Name the blood parasite species.
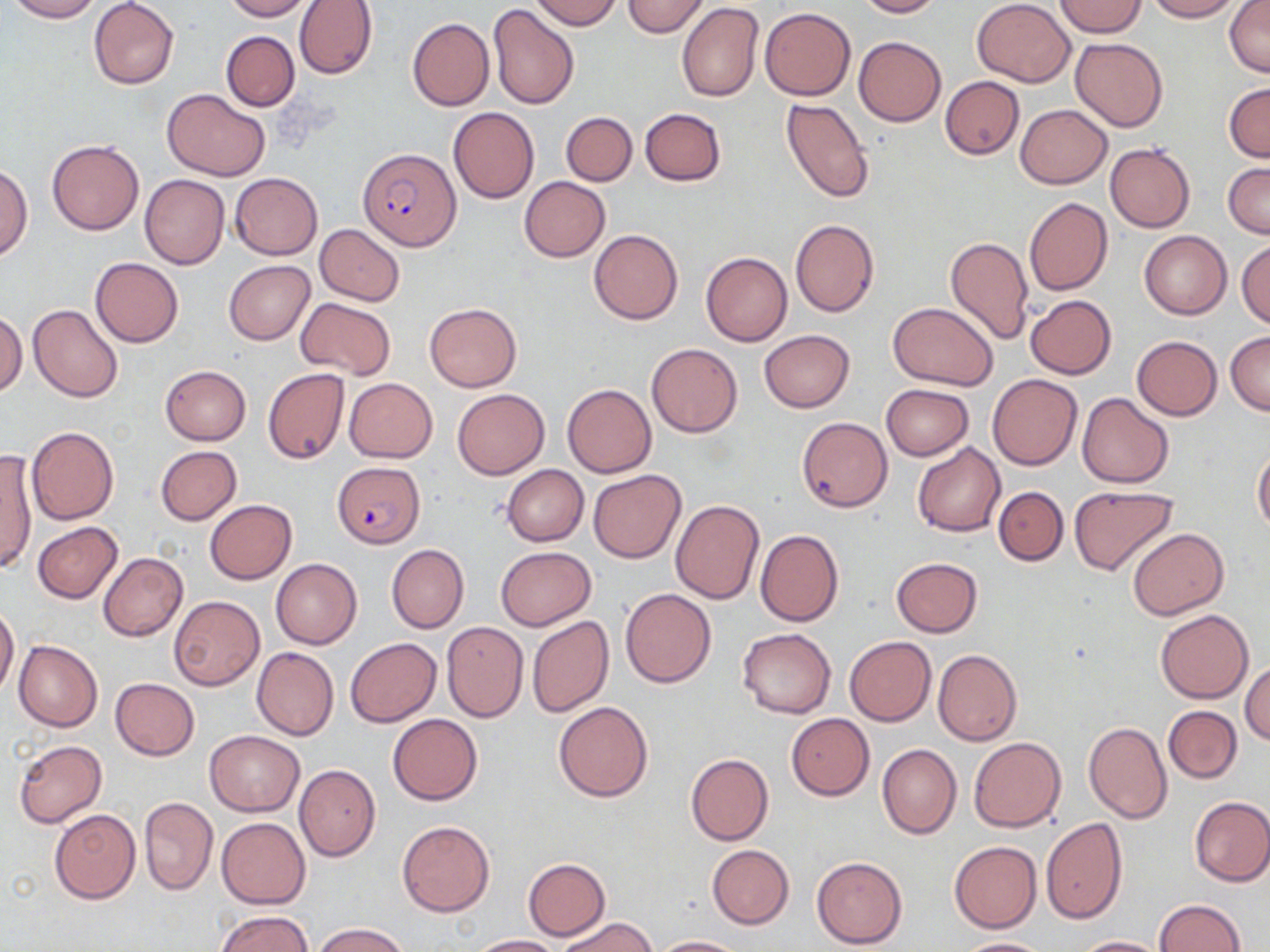

Plasmodium falciparum.

Approximate bounding boxes as named x1/y1/x2/y2 corners in pixels. Plasmodium falciparum-infected red blood cell locations: (x1=360, y1=150, x2=461, y2=251), (x1=331, y1=462, x2=422, y2=544). Uninfected red blood cell locations: (x1=6, y1=0, x2=102, y2=22), (x1=88, y1=0, x2=179, y2=89), (x1=220, y1=0, x2=311, y2=21), (x1=294, y1=0, x2=377, y2=79), (x1=529, y1=0, x2=621, y2=30), (x1=623, y1=0, x2=709, y2=37), (x1=853, y1=0, x2=942, y2=17), (x1=971, y1=0, x2=1076, y2=86), (x1=1145, y1=0, x2=1243, y2=21), (x1=1225, y1=0, x2=1270, y2=76), (x1=1054, y1=1, x2=1147, y2=37), (x1=487, y1=3, x2=579, y2=110), (x1=677, y1=3, x2=764, y2=103), (x1=761, y1=7, x2=856, y2=100), (x1=407, y1=17, x2=494, y2=111), (x1=221, y1=30, x2=299, y2=112), (x1=854, y1=36, x2=946, y2=126), (x1=1071, y1=38, x2=1168, y2=131), (x1=940, y1=76, x2=1025, y2=159), (x1=1224, y1=82, x2=1269, y2=162), (x1=162, y1=88, x2=271, y2=180), (x1=781, y1=97, x2=875, y2=203), (x1=1014, y1=105, x2=1113, y2=189), (x1=448, y1=107, x2=540, y2=203), (x1=640, y1=109, x2=726, y2=185), (x1=561, y1=112, x2=637, y2=185), (x1=47, y1=140, x2=144, y2=234), (x1=1105, y1=143, x2=1195, y2=232), (x1=1224, y1=162, x2=1269, y2=239), (x1=1, y1=164, x2=33, y2=261), (x1=230, y1=172, x2=322, y2=259), (x1=140, y1=174, x2=229, y2=270), (x1=518, y1=176, x2=610, y2=261), (x1=1024, y1=197, x2=1113, y2=295), (x1=790, y1=218, x2=878, y2=317), (x1=315, y1=225, x2=405, y2=305), (x1=590, y1=230, x2=683, y2=324), (x1=1139, y1=231, x2=1232, y2=319), (x1=945, y1=236, x2=1034, y2=344), (x1=1237, y1=239, x2=1270, y2=328), (x1=701, y1=251, x2=793, y2=346), (x1=90, y1=257, x2=183, y2=348), (x1=224, y1=260, x2=315, y2=344), (x1=1025, y1=295, x2=1117, y2=379), (x1=294, y1=298, x2=396, y2=380), (x1=424, y1=302, x2=522, y2=391), (x1=887, y1=302, x2=998, y2=389), (x1=28, y1=303, x2=123, y2=402), (x1=0, y1=312, x2=26, y2=396), (x1=759, y1=330, x2=854, y2=412), (x1=1226, y1=331, x2=1270, y2=415), (x1=1132, y1=335, x2=1223, y2=420), (x1=646, y1=342, x2=743, y2=438), (x1=160, y1=365, x2=251, y2=445), (x1=263, y1=368, x2=350, y2=464), (x1=988, y1=374, x2=1082, y2=470), (x1=343, y1=377, x2=437, y2=462), (x1=562, y1=383, x2=655, y2=477), (x1=881, y1=384, x2=974, y2=460), (x1=453, y1=389, x2=549, y2=479), (x1=1076, y1=393, x2=1174, y2=488), (x1=797, y1=417, x2=892, y2=511), (x1=26, y1=426, x2=119, y2=525), (x1=912, y1=442, x2=1006, y2=537), (x1=155, y1=446, x2=242, y2=524), (x1=1253, y1=448, x2=1270, y2=535), (x1=1, y1=453, x2=35, y2=576), (x1=502, y1=464, x2=588, y2=545), (x1=589, y1=470, x2=686, y2=564), (x1=993, y1=486, x2=1068, y2=565), (x1=1071, y1=486, x2=1178, y2=576), (x1=671, y1=499, x2=765, y2=605), (x1=205, y1=500, x2=297, y2=584), (x1=32, y1=522, x2=123, y2=603), (x1=1127, y1=527, x2=1228, y2=620), (x1=755, y1=529, x2=844, y2=627), (x1=386, y1=544, x2=469, y2=633), (x1=494, y1=547, x2=596, y2=631), (x1=99, y1=553, x2=189, y2=642), (x1=271, y1=558, x2=361, y2=648), (x1=891, y1=558, x2=983, y2=637), (x1=621, y1=588, x2=716, y2=688), (x1=168, y1=595, x2=265, y2=690), (x1=0, y1=605, x2=19, y2=696), (x1=1155, y1=609, x2=1254, y2=702), (x1=526, y1=616, x2=615, y2=718), (x1=442, y1=622, x2=528, y2=721), (x1=737, y1=627, x2=836, y2=718), (x1=845, y1=636, x2=936, y2=725), (x1=345, y1=638, x2=441, y2=727), (x1=14, y1=640, x2=103, y2=732), (x1=252, y1=647, x2=338, y2=740), (x1=932, y1=649, x2=1023, y2=746), (x1=1240, y1=660, x2=1269, y2=746), (x1=110, y1=678, x2=199, y2=760), (x1=554, y1=701, x2=652, y2=802), (x1=1163, y1=706, x2=1241, y2=783), (x1=387, y1=713, x2=482, y2=804), (x1=786, y1=713, x2=874, y2=800), (x1=1083, y1=721, x2=1173, y2=825), (x1=204, y1=730, x2=304, y2=816), (x1=969, y1=738, x2=1066, y2=832), (x1=13, y1=739, x2=107, y2=829), (x1=877, y1=744, x2=962, y2=839), (x1=685, y1=752, x2=774, y2=846), (x1=294, y1=764, x2=380, y2=862), (x1=1189, y1=795, x2=1270, y2=886), (x1=138, y1=796, x2=217, y2=894), (x1=48, y1=809, x2=141, y2=904), (x1=216, y1=816, x2=310, y2=908), (x1=1041, y1=818, x2=1128, y2=924), (x1=398, y1=821, x2=495, y2=916), (x1=949, y1=841, x2=1042, y2=932), (x1=706, y1=844, x2=794, y2=928), (x1=812, y1=856, x2=907, y2=947), (x1=522, y1=858, x2=611, y2=939), (x1=1155, y1=899, x2=1246, y2=952), (x1=214, y1=910, x2=315, y2=952), (x1=554, y1=916, x2=657, y2=952), (x1=312, y1=923, x2=409, y2=952), (x1=469, y1=934, x2=560, y2=952), (x1=650, y1=935, x2=745, y2=952), (x1=1071, y1=936, x2=1165, y2=952), (x1=954, y1=938, x2=1055, y2=952). Optical microscopy. May-Grünwald-Giemsa-stained preparation. Image is 1270×952 pixels. Thin blood smear. Single field of view. 1000x magnification.